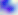
Summary:
  - Magnification: 400x
  - Modality: photomicrograph
  - Identification: Toxoplasma gondii